Report the malaria status of this cell.
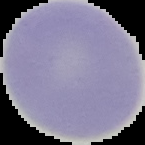
It is uninfected.

From a thin blood smear. Image is 145×145 pixels. The area outside the segmented cell region is set to black.